Comment on the morphology of the erythrocytes.
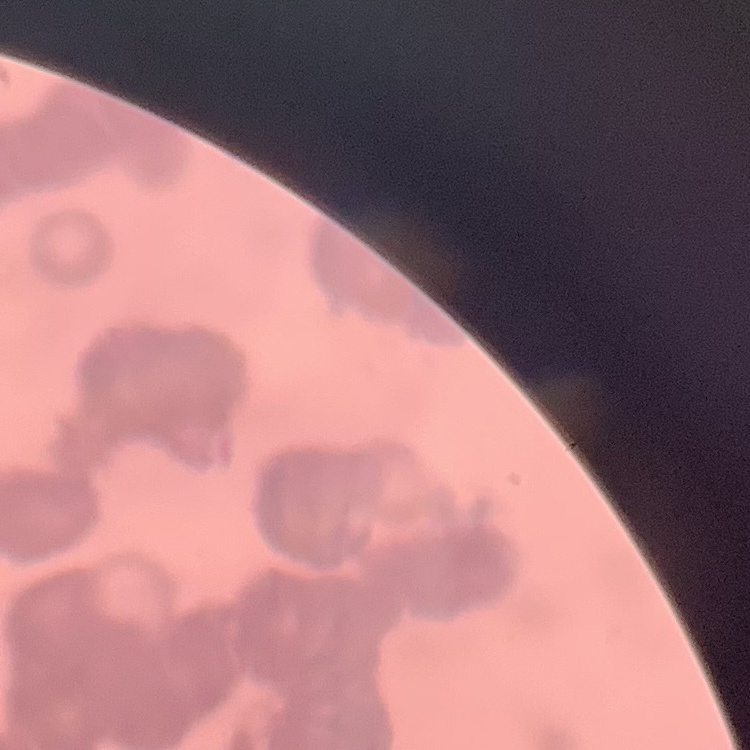

Rouleaux formation.

Summary:
  - Stain: Field's or Giemsa
  - Preparation: thin peripheral smear
  - Image type: square crop of a larger photomicrograph